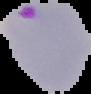
From a thin blood smear. Image is 91×94 pixels. The area outside the segmented cell region is set to black. Malaria status: parasitized.